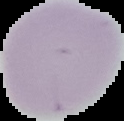

Summary:
  - Image size: 124×121 pixels
  - Image type: cell region segmented out of the field of view; surrounding area masked to black
  - Preparation: thin blood smear
  - Malaria status: uninfected